Locate every blood parasite and identify its species.
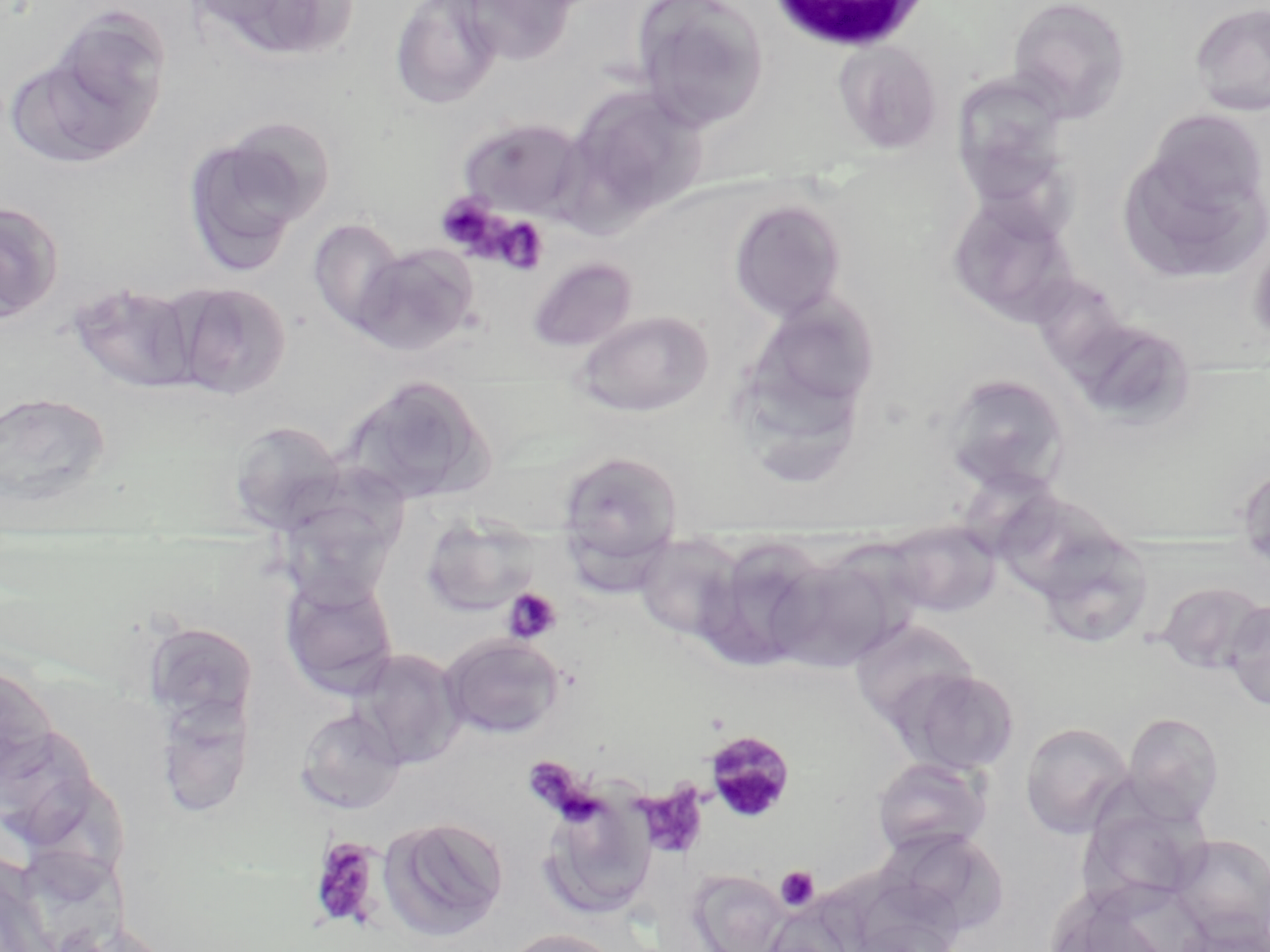

Approximate bounding boxes as (x1, y1, x2, y2) in pixels.
Plasmodium malariae-infected red blood cells: (703, 730, 795, 823).
No Plasmodium falciparum, Plasmodium ovale, Plasmodium vivax, Babesia divergens, or Trypanosoma brucei observed.

Summary:
  - White blood cell locations: (766, 0, 934, 55)
  - Uninfected red blood cell locations: (183, 0, 360, 65), (390, 0, 503, 110), (451, 0, 581, 66), (630, 0, 770, 131), (1007, 0, 1131, 122), (1189, 3, 1270, 117), (48, 6, 172, 127), (832, 40, 942, 154), (4, 52, 153, 170), (951, 74, 1072, 210), (566, 85, 710, 224), (215, 113, 339, 230), (455, 116, 589, 220), (181, 129, 317, 276), (1115, 132, 1269, 285), (945, 192, 1079, 325), (728, 198, 847, 322), (0, 201, 65, 324), (306, 217, 406, 335), (1247, 234, 1270, 350), (351, 243, 479, 356), (526, 256, 638, 354), (68, 281, 203, 394), (167, 281, 291, 400), (741, 293, 881, 431), (571, 309, 715, 418), (1073, 332, 1206, 431), (939, 373, 1071, 497), (341, 374, 495, 506), (0, 389, 114, 511), (228, 420, 346, 533), (556, 450, 685, 572), (1238, 465, 1270, 574), (420, 513, 543, 616), (886, 520, 1001, 617), (1033, 529, 1154, 650), (633, 534, 744, 642), (699, 537, 832, 672), (768, 548, 906, 674), (279, 572, 399, 699), (1154, 580, 1267, 674), (1223, 600, 1270, 711), (849, 619, 978, 729), (142, 621, 258, 727), (439, 632, 565, 740), (348, 647, 466, 770), (0, 661, 61, 794), (895, 667, 1021, 777), (153, 693, 256, 819), (295, 706, 407, 814), (1122, 711, 1225, 821), (1020, 722, 1134, 839), (0, 728, 99, 849), (871, 756, 992, 859), (1090, 765, 1228, 909), (538, 792, 657, 921), (378, 815, 508, 940), (874, 827, 1008, 937), (1170, 833, 1270, 944), (22, 849, 128, 947), (686, 869, 789, 952), (1177, 912, 1268, 952), (501, 928, 626, 952)
  - Platelet locations: (436, 193, 503, 254), (493, 216, 549, 276), (501, 587, 562, 644), (639, 783, 708, 858), (308, 836, 385, 931), (775, 866, 819, 911)
  - Slide-level diagnosis: Plasmodium malariae
  - Magnification: 1000x
  - Stain: May-Grünwald-Giemsa
  - Preparation: thin blood smear
  - Field of view: single
  - Modality: light microscopy
  - Image size: 1270×952 pixels